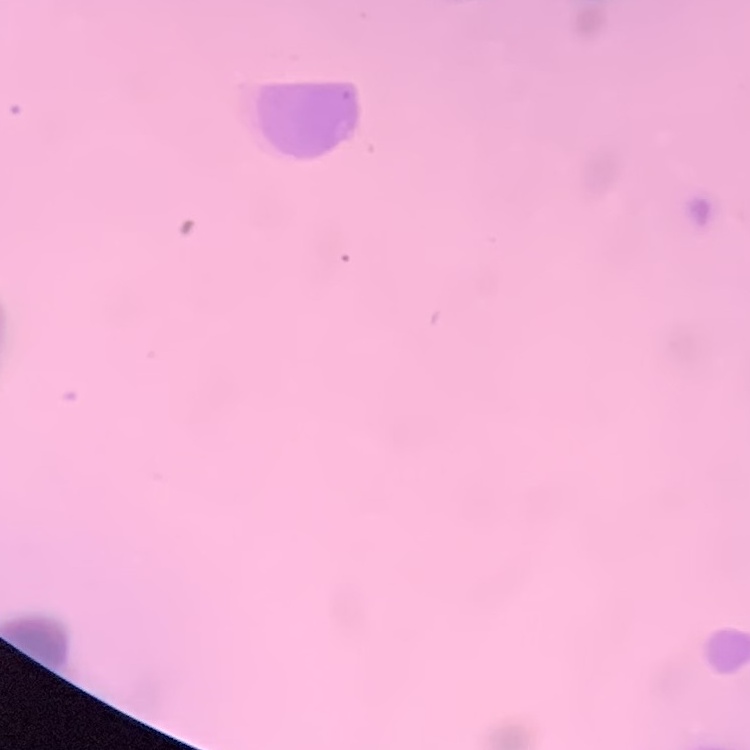
The erythrocytes show rouleaux formation. Field's or Giemsa stain. Thin peripheral smear. Square crop of a larger photomicrograph.